State which parasite is depicted.
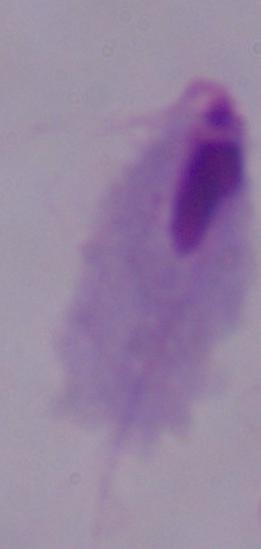

A trichomonad.

Summary:
  - Modality: micrograph
  - Magnification: 1000x